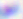
identification = Toxoplasma gondii
magnification = 400x
modality = photomicrograph